Assess this cell for malaria.
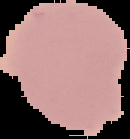

Uninfected.

Summary:
  - Preparation: thin blood smear
  - Image type: cell region segmented out of the field of view; surrounding area masked to black
  - Image size: 130×139 pixels